Name the blood parasite species.
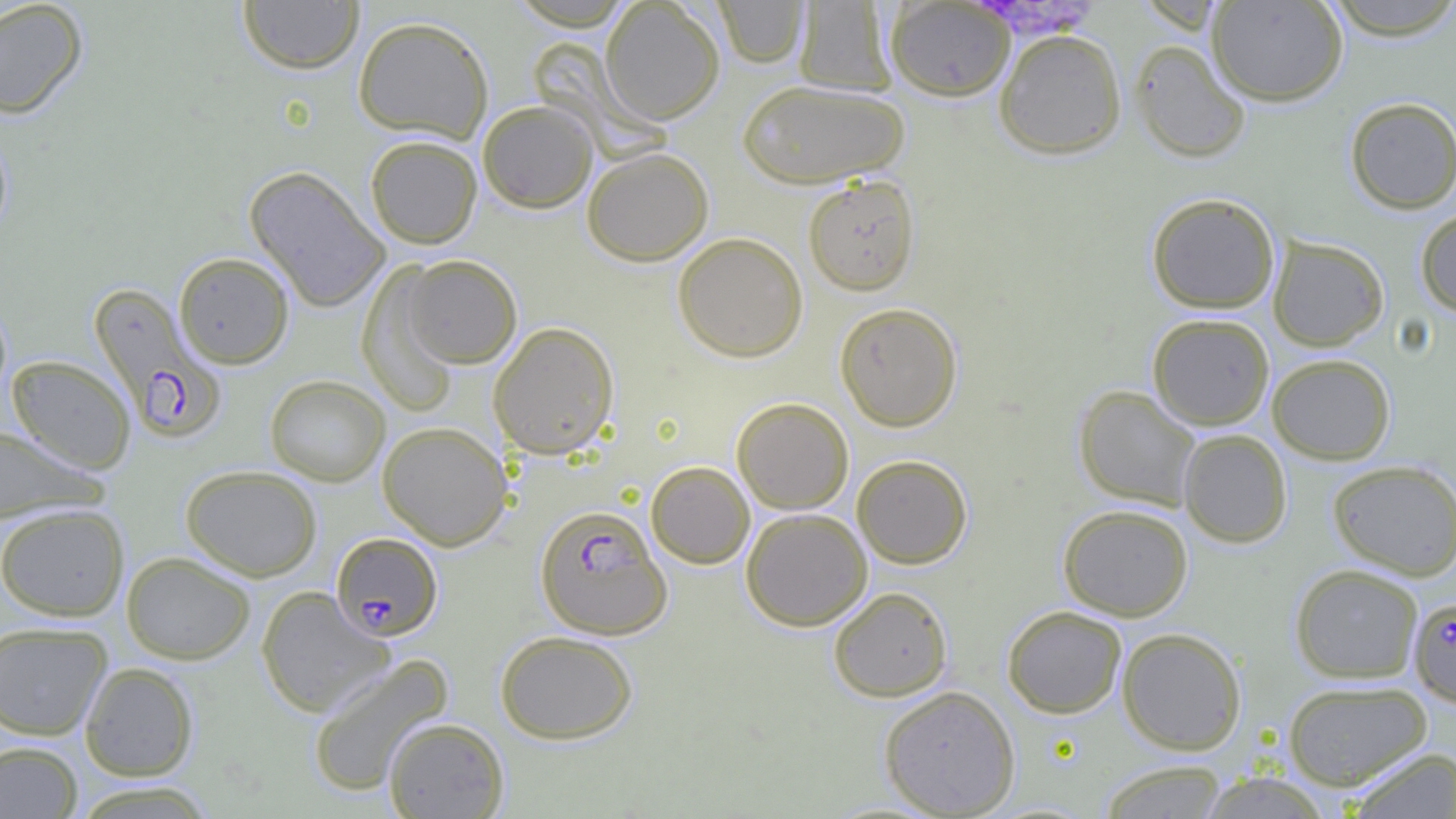
Plasmodium falciparum.

Approximate bounding boxes as named x1/y1/x2/y2 corners in pixels. Plasmodium falciparum-infected red blood cell locations: (x1=88, y1=282, x2=227, y2=444), (x1=535, y1=503, x2=671, y2=640), (x1=331, y1=532, x2=444, y2=641), (x1=1408, y1=596, x2=1456, y2=707). Uninfected red blood cell locations: (x1=0, y1=0, x2=88, y2=118), (x1=238, y1=0, x2=365, y2=74), (x1=1207, y1=0, x2=1348, y2=106), (x1=1319, y1=0, x2=1456, y2=40), (x1=714, y1=1, x2=809, y2=68), (x1=793, y1=1, x2=897, y2=97), (x1=885, y1=1, x2=1015, y2=101), (x1=600, y1=2, x2=725, y2=124), (x1=353, y1=15, x2=494, y2=142), (x1=994, y1=29, x2=1127, y2=160), (x1=1130, y1=39, x2=1251, y2=164), (x1=737, y1=79, x2=910, y2=188), (x1=1344, y1=96, x2=1456, y2=214), (x1=478, y1=100, x2=598, y2=213), (x1=0, y1=127, x2=13, y2=240), (x1=365, y1=135, x2=482, y2=249), (x1=581, y1=146, x2=714, y2=266), (x1=244, y1=166, x2=390, y2=312), (x1=802, y1=174, x2=921, y2=295), (x1=1146, y1=192, x2=1280, y2=313), (x1=1415, y1=208, x2=1456, y2=318), (x1=672, y1=232, x2=809, y2=362), (x1=1267, y1=235, x2=1389, y2=351), (x1=174, y1=252, x2=294, y2=369), (x1=400, y1=254, x2=522, y2=368), (x1=357, y1=263, x2=462, y2=417), (x1=834, y1=302, x2=963, y2=431), (x1=1147, y1=313, x2=1275, y2=430), (x1=488, y1=321, x2=620, y2=459), (x1=1267, y1=353, x2=1395, y2=464), (x1=6, y1=355, x2=136, y2=473), (x1=265, y1=375, x2=390, y2=487), (x1=1073, y1=384, x2=1202, y2=511), (x1=732, y1=397, x2=854, y2=514), (x1=377, y1=421, x2=512, y2=550), (x1=0, y1=425, x2=104, y2=523), (x1=1178, y1=429, x2=1292, y2=547), (x1=852, y1=454, x2=973, y2=568), (x1=1326, y1=459, x2=1456, y2=580), (x1=645, y1=460, x2=755, y2=569), (x1=180, y1=465, x2=322, y2=581), (x1=0, y1=503, x2=129, y2=621), (x1=1058, y1=504, x2=1193, y2=621), (x1=741, y1=508, x2=872, y2=631), (x1=122, y1=551, x2=256, y2=664), (x1=1289, y1=563, x2=1424, y2=683), (x1=256, y1=586, x2=395, y2=718), (x1=828, y1=586, x2=953, y2=702), (x1=1002, y1=605, x2=1127, y2=718), (x1=0, y1=621, x2=113, y2=740), (x1=1117, y1=627, x2=1247, y2=755), (x1=495, y1=630, x2=638, y2=744), (x1=306, y1=654, x2=454, y2=797), (x1=80, y1=662, x2=199, y2=781), (x1=1282, y1=679, x2=1432, y2=790), (x1=878, y1=685, x2=1021, y2=817), (x1=383, y1=717, x2=509, y2=818), (x1=0, y1=741, x2=83, y2=819), (x1=1345, y1=746, x2=1456, y2=819), (x1=1097, y1=760, x2=1229, y2=818), (x1=1196, y1=771, x2=1335, y2=817), (x1=68, y1=781, x2=220, y2=819). Light microscopy. Thin blood film. 1000x magnification. Single field of view. Image is 1456×819 pixels.